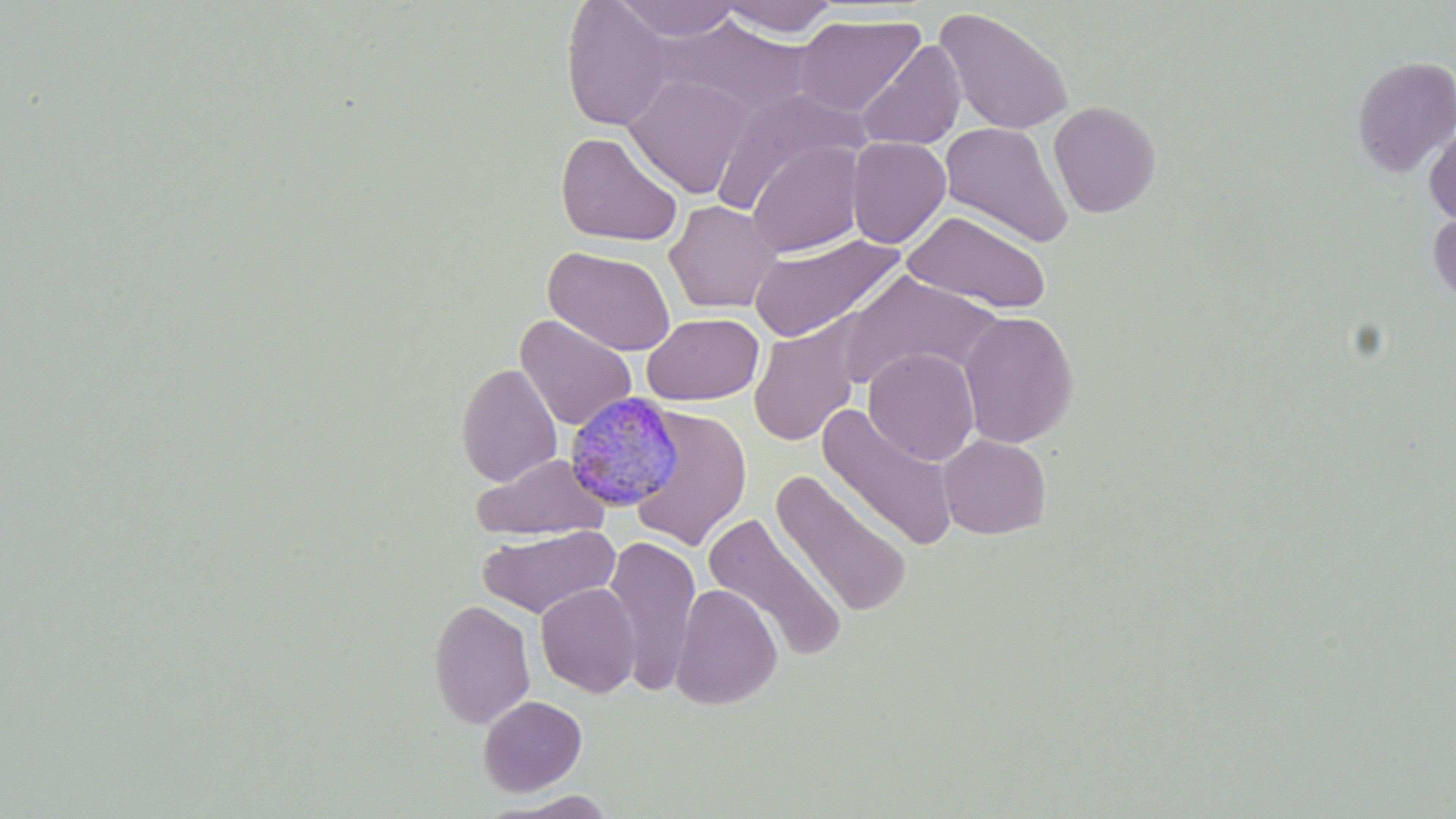

slide-level diagnosis = Plasmodium malariae
preparation = thin blood smear
magnification = 1000x
uninfected red blood cell locations = approximate bounding boxes as [x1, y1, x2, y2] in pixels: [614, 0, 743, 41], [561, 1, 673, 131], [717, 1, 840, 38], [934, 6, 1075, 137], [793, 13, 926, 117], [651, 14, 814, 119], [674, 31, 848, 194], [855, 39, 966, 152], [1352, 56, 1456, 176], [623, 73, 755, 199], [712, 88, 868, 215], [1048, 100, 1161, 218], [939, 121, 1074, 248], [1424, 123, 1456, 226], [555, 130, 684, 248], [846, 137, 951, 248], [746, 140, 865, 258], [664, 199, 781, 314], [1428, 208, 1456, 306], [902, 210, 1051, 314], [746, 232, 905, 344], [543, 246, 676, 356], [833, 271, 1003, 390], [958, 310, 1079, 448], [642, 313, 763, 405], [516, 315, 637, 431], [748, 319, 865, 446], [864, 348, 980, 465], [456, 362, 562, 487], [629, 405, 753, 551], [817, 405, 960, 552], [938, 434, 1051, 539], [471, 453, 610, 542], [770, 470, 913, 618], [702, 512, 849, 662], [478, 524, 620, 619], [603, 536, 701, 695], [535, 583, 640, 698], [670, 583, 783, 711], [428, 598, 535, 729], [477, 695, 587, 796], [487, 791, 621, 818]
stain = May-Grünwald-Giemsa
modality = light microscopy
image size = 1456×819 pixels
field of view = single
Plasmodium malariae-infected red blood cell locations = approximate bounding boxes as [x1, y1, x2, y2] in pixels: [562, 389, 684, 513]